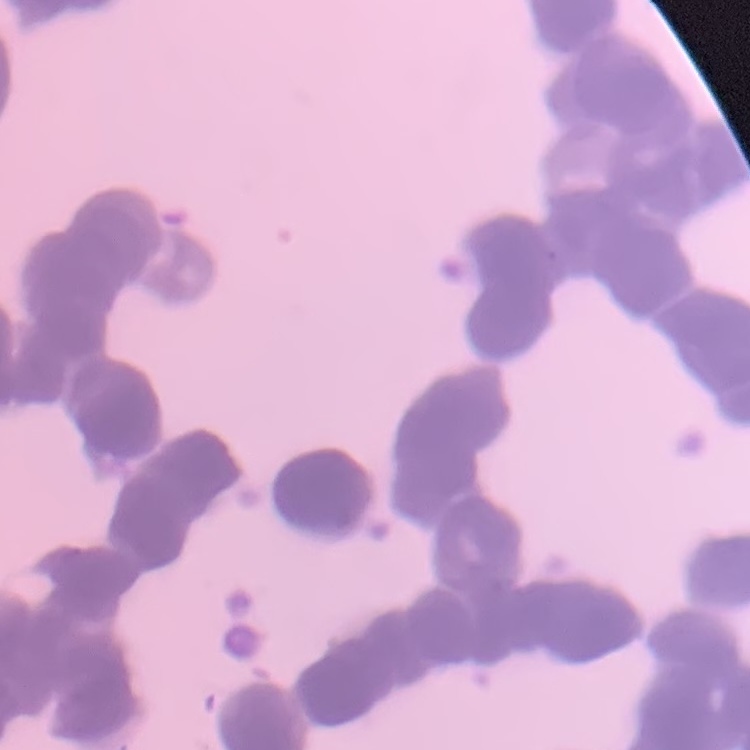
erythrocyte morphology = rouleaux formation
preparation = thin blood smear
stain = Field's or Giemsa
image type = one tile cut from a larger photomicrograph